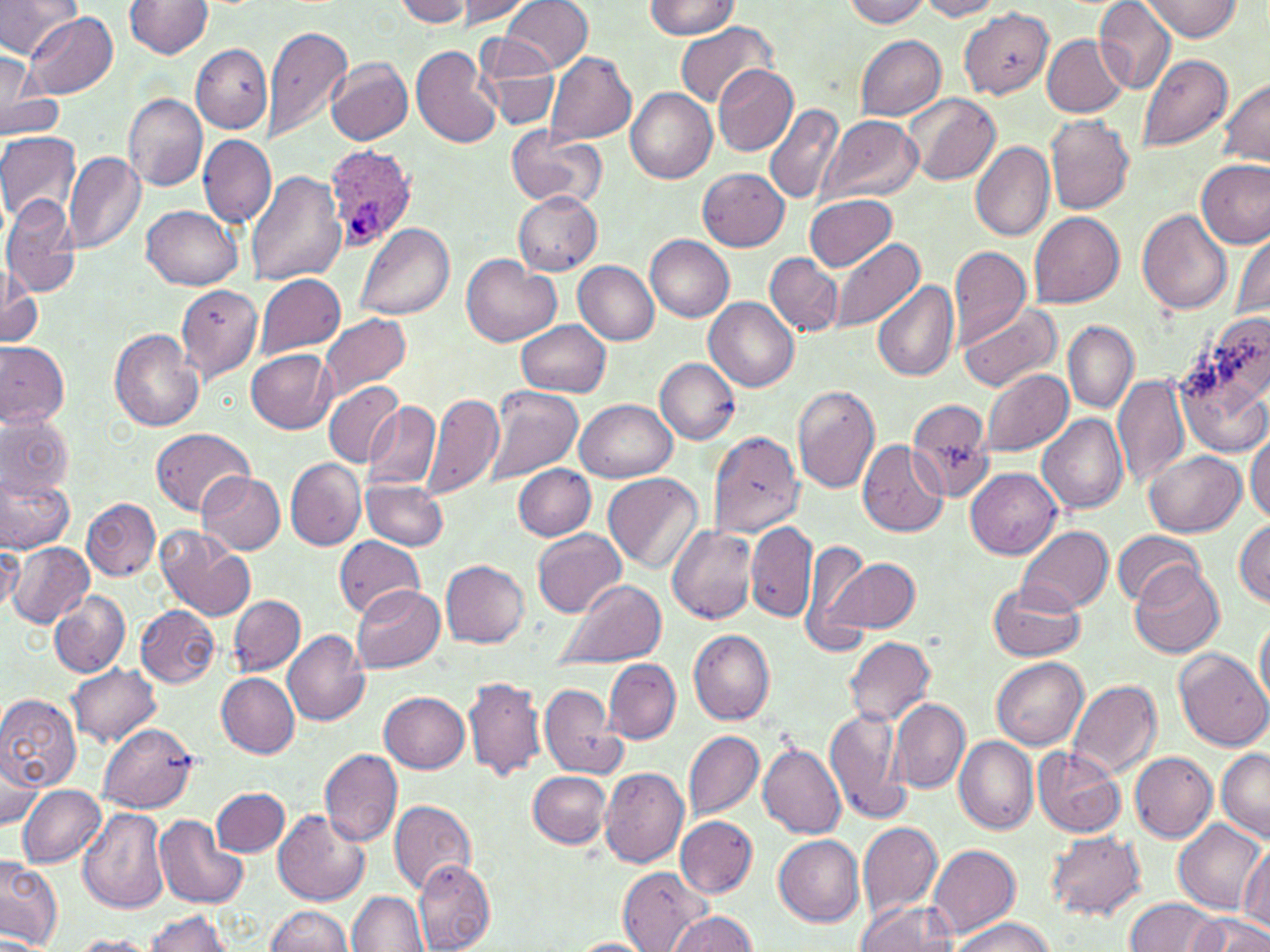
slide_level_diagnosis: Plasmodium ovale
uninfected_red_blood_cell_locations: 'approximate bounding boxes as named x1/y1/x2/y2 corners in pixels: (x1=0, y1=0, x2=80, y2=57), (x1=125, y1=0, x2=214, y2=57), (x1=395, y1=0, x2=473, y2=27), (x1=501, y1=0, x2=592, y2=73), (x1=842, y1=0, x2=930, y2=27), (x1=916, y1=0, x2=1006, y2=20), (x1=1095, y1=0, x2=1177, y2=93), (x1=1138, y1=0, x2=1241, y2=41), (x1=459, y1=1, x2=534, y2=25), (x1=644, y1=1, x2=740, y2=37), (x1=960, y1=7, x2=1054, y2=98), (x1=22, y1=12, x2=119, y2=98), (x1=673, y1=22, x2=775, y2=111), (x1=261, y1=24, x2=353, y2=144), (x1=1042, y1=34, x2=1128, y2=117), (x1=475, y1=35, x2=562, y2=131), (x1=854, y1=35, x2=948, y2=121), (x1=191, y1=43, x2=273, y2=132), (x1=411, y1=44, x2=501, y2=148), (x1=2, y1=50, x2=43, y2=133), (x1=545, y1=50, x2=637, y2=147), (x1=1136, y1=52, x2=1234, y2=154), (x1=327, y1=58, x2=413, y2=147), (x1=712, y1=62, x2=798, y2=156), (x1=1216, y1=77, x2=1270, y2=165), (x1=0, y1=85, x2=63, y2=140), (x1=626, y1=87, x2=717, y2=182), (x1=122, y1=92, x2=207, y2=192), (x1=901, y1=93, x2=1001, y2=186), (x1=764, y1=103, x2=845, y2=203), (x1=819, y1=114, x2=923, y2=205), (x1=1044, y1=115, x2=1134, y2=214), (x1=503, y1=126, x2=606, y2=211), (x1=0, y1=130, x2=82, y2=225), (x1=198, y1=134, x2=275, y2=229), (x1=971, y1=140, x2=1055, y2=241), (x1=63, y1=150, x2=146, y2=256), (x1=1197, y1=158, x2=1269, y2=247), (x1=697, y1=168, x2=789, y2=250), (x1=246, y1=171, x2=346, y2=287), (x1=513, y1=192, x2=603, y2=276), (x1=805, y1=194, x2=899, y2=271), (x1=1, y1=195, x2=82, y2=297), (x1=142, y1=206, x2=243, y2=290), (x1=1137, y1=208, x2=1231, y2=315), (x1=1029, y1=211, x2=1125, y2=308), (x1=358, y1=222, x2=455, y2=322), (x1=1232, y1=231, x2=1270, y2=325), (x1=645, y1=235, x2=734, y2=322), (x1=829, y1=238, x2=926, y2=336), (x1=948, y1=245, x2=1033, y2=345), (x1=765, y1=252, x2=845, y2=336), (x1=461, y1=256, x2=561, y2=347), (x1=573, y1=261, x2=659, y2=344), (x1=0, y1=264, x2=41, y2=350), (x1=254, y1=275, x2=346, y2=358), (x1=872, y1=279, x2=960, y2=381), (x1=175, y1=284, x2=263, y2=383), (x1=704, y1=298, x2=800, y2=391), (x1=958, y1=302, x2=1063, y2=393), (x1=318, y1=313, x2=411, y2=398), (x1=518, y1=320, x2=611, y2=397), (x1=1063, y1=322, x2=1138, y2=413), (x1=109, y1=328, x2=205, y2=432), (x1=1175, y1=328, x2=1270, y2=457), (x1=0, y1=342, x2=69, y2=430), (x1=247, y1=349, x2=337, y2=433), (x1=655, y1=358, x2=741, y2=445), (x1=980, y1=367, x2=1072, y2=457), (x1=1112, y1=375, x2=1188, y2=487), (x1=322, y1=380, x2=403, y2=468), (x1=482, y1=385, x2=582, y2=488), (x1=791, y1=386, x2=881, y2=494), (x1=424, y1=392, x2=503, y2=500), (x1=906, y1=396, x2=996, y2=503), (x1=575, y1=399, x2=677, y2=482), (x1=365, y1=401, x2=441, y2=491), (x1=0, y1=409, x2=75, y2=500), (x1=1038, y1=412, x2=1128, y2=515), (x1=152, y1=428, x2=255, y2=516), (x1=1245, y1=430, x2=1269, y2=523), (x1=704, y1=431, x2=807, y2=542), (x1=858, y1=440, x2=950, y2=536), (x1=1146, y1=450, x2=1247, y2=538), (x1=285, y1=457, x2=365, y2=550), (x1=512, y1=463, x2=595, y2=541), (x1=966, y1=467, x2=1062, y2=560), (x1=603, y1=472, x2=704, y2=573), (x1=198, y1=473, x2=285, y2=555), (x1=0, y1=474, x2=75, y2=552), (x1=362, y1=479, x2=449, y2=550), (x1=83, y1=498, x2=160, y2=580), (x1=1234, y1=518, x2=1270, y2=605), (x1=746, y1=521, x2=816, y2=621), (x1=153, y1=525, x2=256, y2=622), (x1=1016, y1=525, x2=1114, y2=614), (x1=667, y1=526, x2=758, y2=624), (x1=531, y1=528, x2=627, y2=616), (x1=1112, y1=531, x2=1203, y2=605), (x1=333, y1=537, x2=423, y2=618), (x1=801, y1=539, x2=871, y2=651), (x1=7, y1=540, x2=94, y2=628), (x1=0, y1=544, x2=22, y2=619), (x1=825, y1=557, x2=919, y2=633), (x1=441, y1=560, x2=529, y2=647), (x1=1132, y1=563, x2=1225, y2=657), (x1=553, y1=579, x2=667, y2=670), (x1=989, y1=581, x2=1086, y2=661), (x1=352, y1=585, x2=444, y2=673), (x1=50, y1=590, x2=130, y2=677), (x1=229, y1=595, x2=305, y2=675), (x1=136, y1=606, x2=219, y2=688), (x1=1255, y1=611, x2=1270, y2=709), (x1=690, y1=629, x2=776, y2=724), (x1=283, y1=630, x2=369, y2=725), (x1=843, y1=636, x2=937, y2=727), (x1=1176, y1=649, x2=1269, y2=750), (x1=992, y1=657, x2=1088, y2=748), (x1=604, y1=659, x2=680, y2=744), (x1=69, y1=664, x2=161, y2=745), (x1=216, y1=672, x2=299, y2=758), (x1=464, y1=675, x2=546, y2=780), (x1=1065, y1=680, x2=1162, y2=781), (x1=538, y1=683, x2=624, y2=779), (x1=379, y1=691, x2=468, y2=772), (x1=0, y1=693, x2=81, y2=792), (x1=888, y1=697, x2=969, y2=793), (x1=825, y1=705, x2=910, y2=825), (x1=98, y1=722, x2=197, y2=813), (x1=683, y1=729, x2=764, y2=820), (x1=954, y1=736, x2=1038, y2=834), (x1=757, y1=740, x2=847, y2=838), (x1=1032, y1=747, x2=1126, y2=836), (x1=318, y1=748, x2=402, y2=848), (x1=1216, y1=748, x2=1270, y2=842), (x1=1, y1=751, x2=44, y2=831), (x1=1129, y1=751, x2=1218, y2=842), (x1=599, y1=766, x2=689, y2=868), (x1=530, y1=770, x2=612, y2=848), (x1=17, y1=784, x2=108, y2=868), (x1=211, y1=786, x2=289, y2=857), (x1=389, y1=799, x2=477, y2=894), (x1=79, y1=806, x2=170, y2=915), (x1=273, y1=810, x2=370, y2=907), (x1=156, y1=815, x2=248, y2=909), (x1=676, y1=816, x2=757, y2=897), (x1=1173, y1=819, x2=1267, y2=914), (x1=857, y1=820, x2=944, y2=918), (x1=1046, y1=830, x2=1145, y2=919), (x1=773, y1=835, x2=864, y2=925), (x1=927, y1=844, x2=1020, y2=940), (x1=1238, y1=847, x2=1270, y2=932), (x1=0, y1=856, x2=62, y2=950), (x1=413, y1=858, x2=496, y2=952), (x1=618, y1=866, x2=711, y2=952), (x1=347, y1=891, x2=429, y2=952), (x1=1124, y1=895, x2=1223, y2=952), (x1=856, y1=899, x2=957, y2=952), (x1=264, y1=906, x2=353, y2=952), (x1=669, y1=910, x2=758, y2=951), (x1=142, y1=911, x2=235, y2=951), (x1=1190, y1=911, x2=1269, y2=952), (x1=952, y1=916, x2=1052, y2=952), (x1=71, y1=936, x2=157, y2=952), (x1=571, y1=937, x2=656, y2=952)'
plasmodium_ovale_infected_red_blood_cell_locations: 'approximate bounding boxes as named x1/y1/x2/y2 corners in pixels: (x1=323, y1=146, x2=419, y2=250)'
magnification: 1000x
stain: May-Grünwald-Giemsa
modality: light microscopy
image_size: 1270×952 pixels
field_of_view: single
preparation: thin blood film